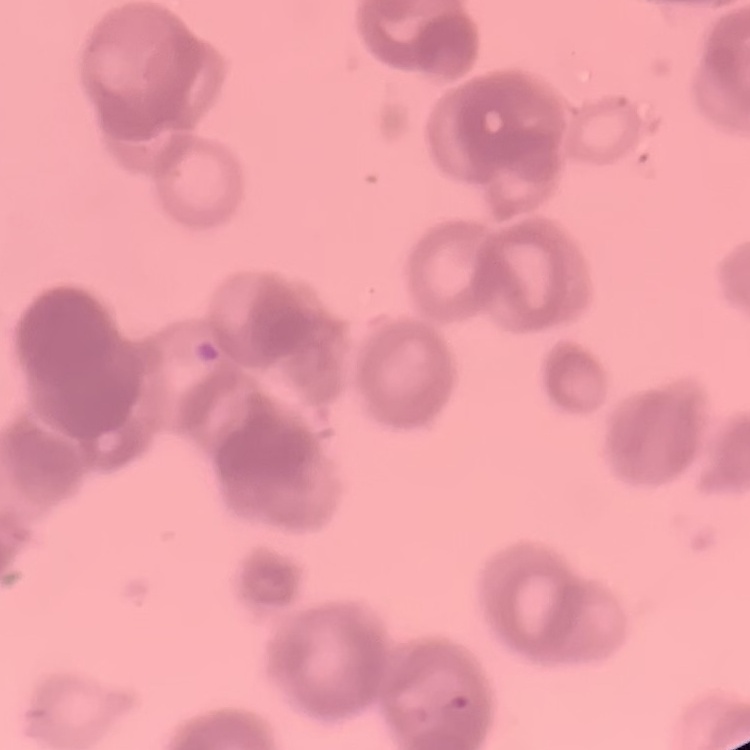

Summary:
  - Red blood cell morphology: rouleaux formation
  - Preparation: thin blood smear
  - Stain: Field's or Giemsa
  - Image type: square crop of a larger photomicrograph